Identify the parasite.
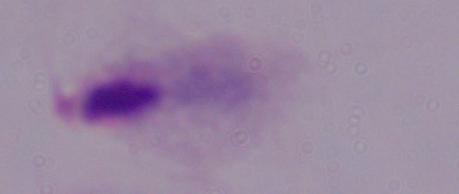

A trichomonad.

Captured at 1000x magnification. Micrograph.